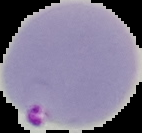 Image is 142×133 pixels. From a thin blood smear. Cell region segmented out of the field of view; the surrounding area is masked to black. Result: malaria parasites identified.